Name the cell type shown.
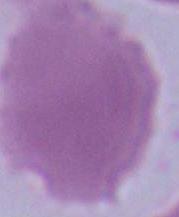
An erythrocyte.

Photomicrograph. 1000x magnification.